Assess this cell for malaria.
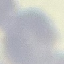
It is uninfected.

image_type: automatically extracted cell patch, resized to 64 × 64 pixels
stain: Giemsa
capture: smartphone through the microscope eyepiece
preparation: thin smear